Rate the background quality.
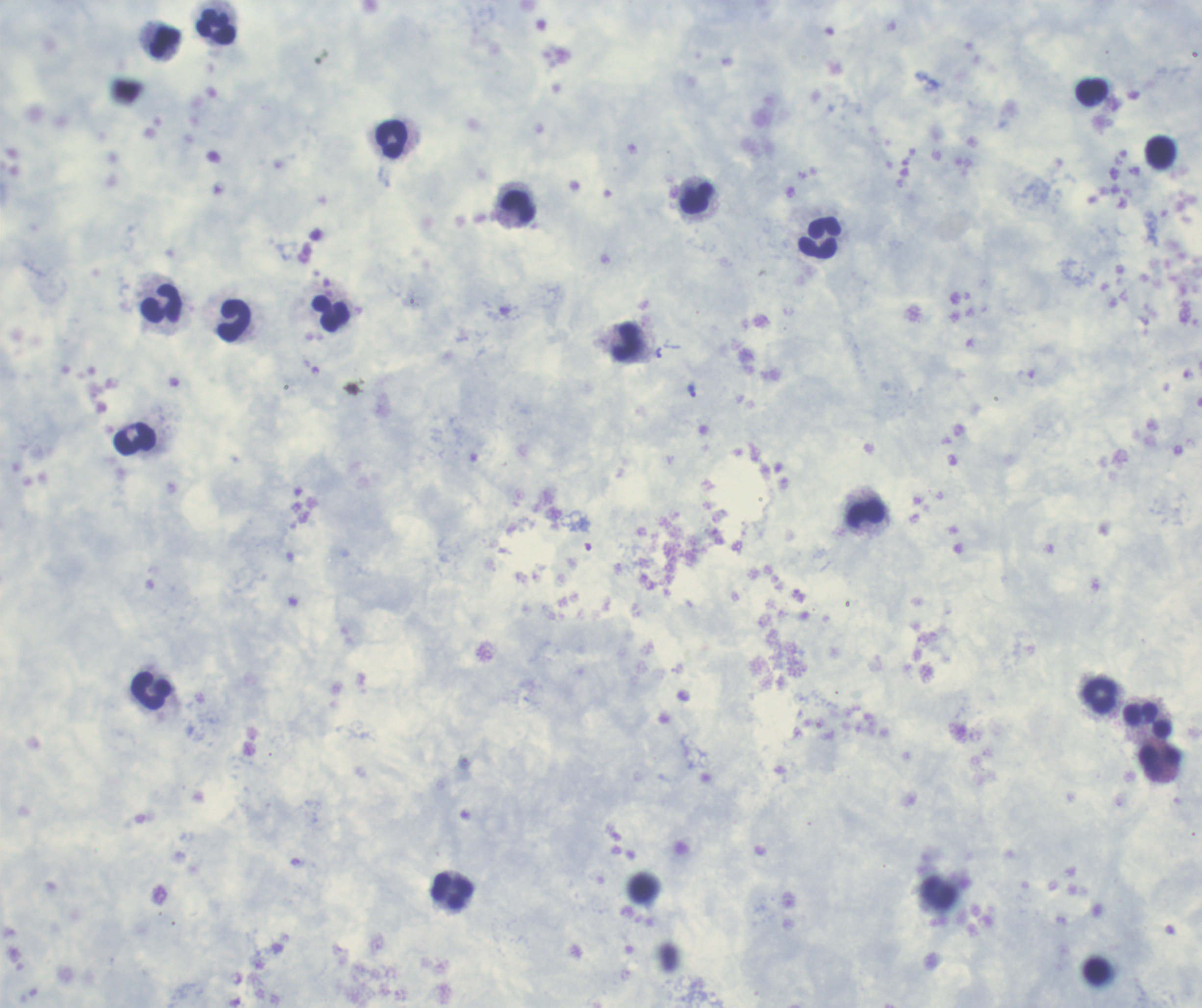

It is good.

{
  "magnification": "100x",
  "preparation": "thick blood film",
  "result": "positive for Plasmodium parasites",
  "context": "previously used in a real diagnosis",
  "field_of_view": "single",
  "image_size": "1202×1008 pixels",
  "trophozoite_locations": "approximate object centers, in pixels from the top-left corner: (x=691, y=390)",
  "coloration_quality": "good",
  "leukocyte_locations": "approximate object centers, in pixels from the top-left corner: (x=216, y=26), (x=165, y=41), (x=1092, y=92), (x=391, y=139), (x=1160, y=152), (x=696, y=197), (x=518, y=207), (x=820, y=237), (x=161, y=303), (x=331, y=313), (x=234, y=320), (x=625, y=342), (x=134, y=438), (x=866, y=514), (x=151, y=691), (x=1099, y=696), (x=1147, y=720), (x=1160, y=755), (x=452, y=890), (x=938, y=892)",
  "stain": "Romanowsky"
}